Name the parasite shown.
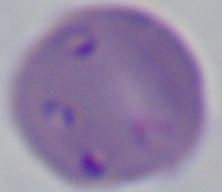
Babesia.

Summary:
  - Modality: micrograph
  - Magnification: 1000x